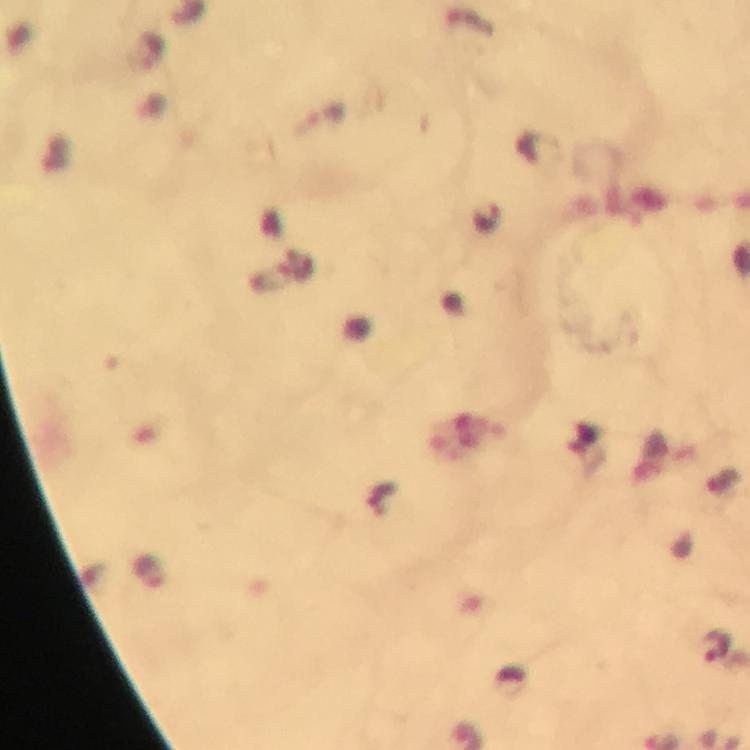

Approximate centers as {x, y} in pixels.
Summary:
  - Plasmodium parasite locations: {325, 115}, {716, 647}
  - Image size: 750×750 pixels
  - Preparation: thick smear
  - Magnification: 100x
  - Immersion oil: used
  - Cropped from: one field of view
  - Stain: Giemsa
  - Context: from a diagnostic examination for malaria
  - Capture: smartphone camera through the microscope